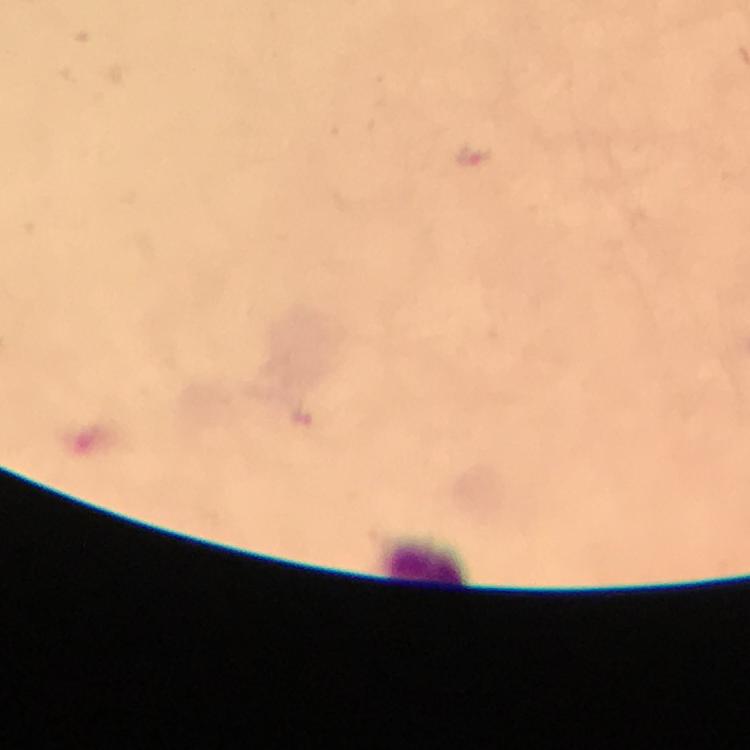 Approximate centers as (x, y) in pixels. Leukocyte locations: (427, 564). Thick smear. From a diagnostic examination for malaria. Image is 750×750 pixels. 100x magnification. Immersion oil was used. Photographed with a smartphone mounted on the microscope. Cropped region of a single field of view. Plasmodium parasites: none seen. Giemsa-stained preparation.